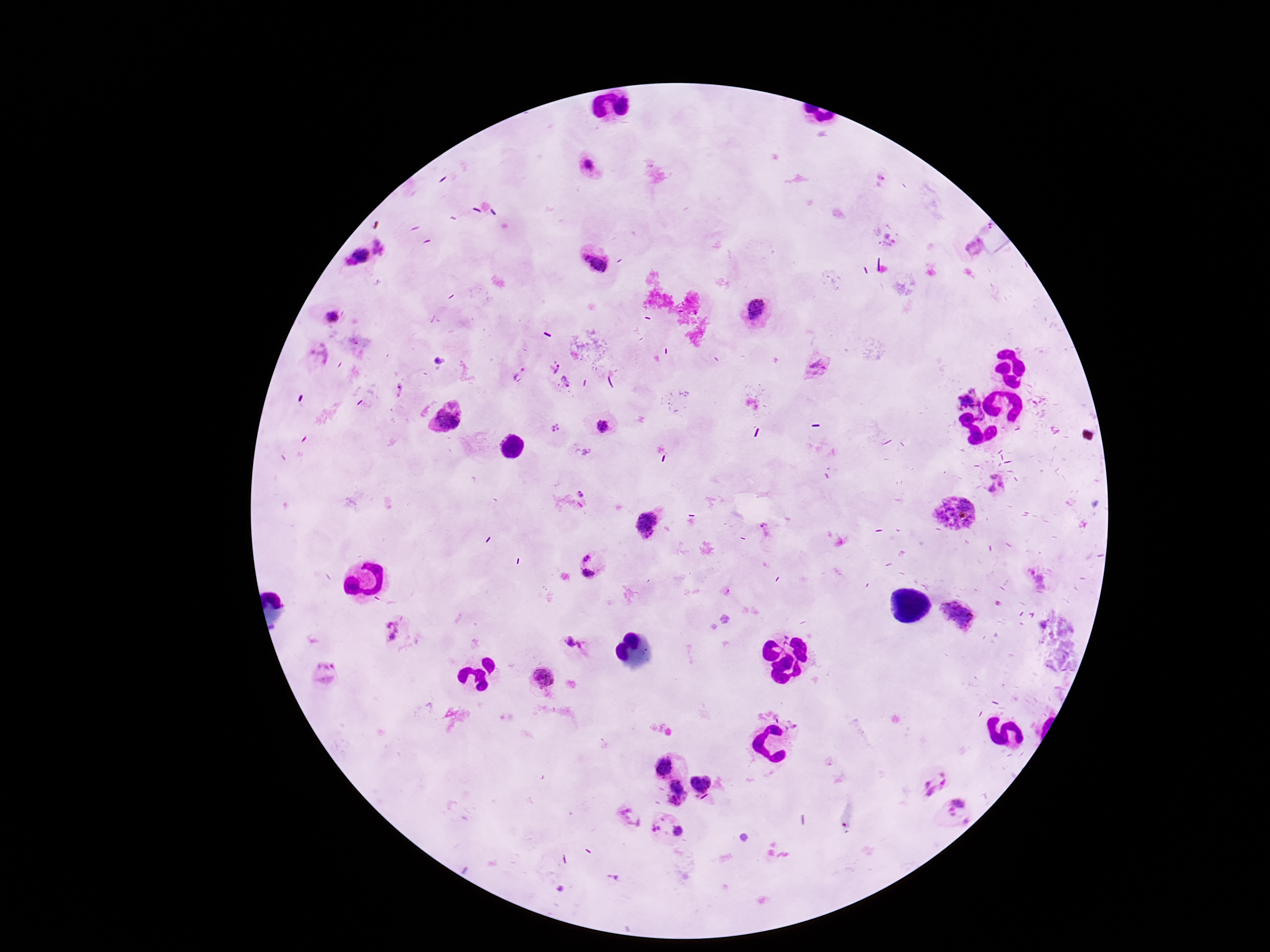
Approximate centers as {x, y} in pixels. Plasmodium parasite locations: {590, 164}, {971, 248}, {357, 258}, {596, 259}, {755, 313}, {333, 316}, {318, 354}, {817, 364}, {555, 369}, {517, 373}, {566, 381}, {964, 399}, {447, 417}, {604, 426}, {556, 427}, {998, 483}, {585, 494}, {954, 518}, {648, 522}, {587, 557}, {588, 573}, {1042, 583}, {396, 631}, {576, 645}, {326, 674}, {545, 676}, {664, 765}, {935, 782}, {703, 783}, {677, 793}, {956, 813}, {632, 816}, {658, 823}, {678, 830}. Thick blood smear. Patient malaria status: infected. Smartphone photograph taken through the microscope eyepiece. Giemsa-stained preparation. Image is 1270×952 pixels. 100x magnification. Single field of view.